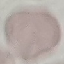

Summary:
  - Result: no malaria parasites seen
  - Preparation: thin smear
  - Image type: cell patch, automatically extracted from a larger field of view and resized to 64 × 64 pixels
  - Stain: Giemsa
  - Capture: smartphone camera at the microscope eyepiece